Describe the morphology of the erythrocytes.
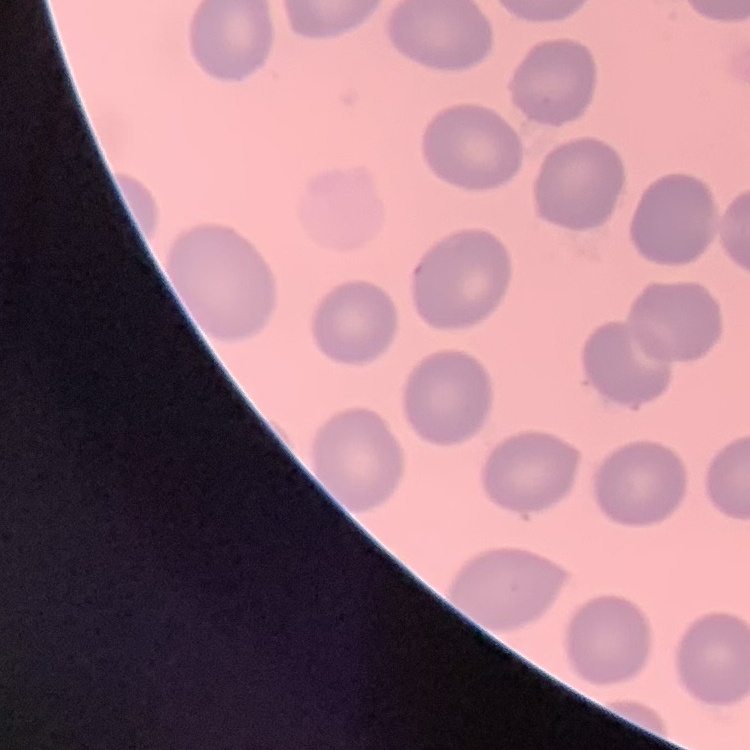

They show no rouleaux formation.

Thin blood film. Square crop of a larger photomicrograph. Stained with either Field's or Giemsa.